Assess this cell for malaria.
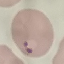
Parasitized.

Acquired by smartphone through the microscope eyepiece. Thin smear of blood. Cell patch, automatically extracted from a larger field of view and resized to 64 × 64 pixels. Giemsa-stained preparation.